Classify this cell by malaria status.
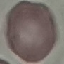
Uninfected.

Acquired by smartphone through the microscope eyepiece. Thin blood film. Automatically extracted cell patch, resized to 64 × 64 pixels. Giemsa-stained preparation.